Assess the morphology of the red blood cells.
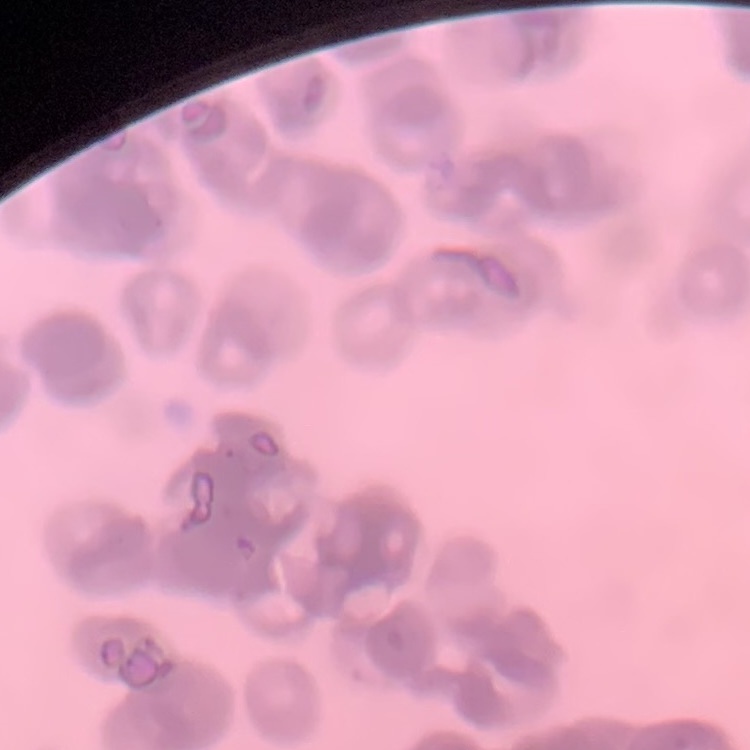
Rouleaux formation.

image type = one tile cut from a larger photomicrograph
stain = Field's or Giemsa
preparation = thin blood film